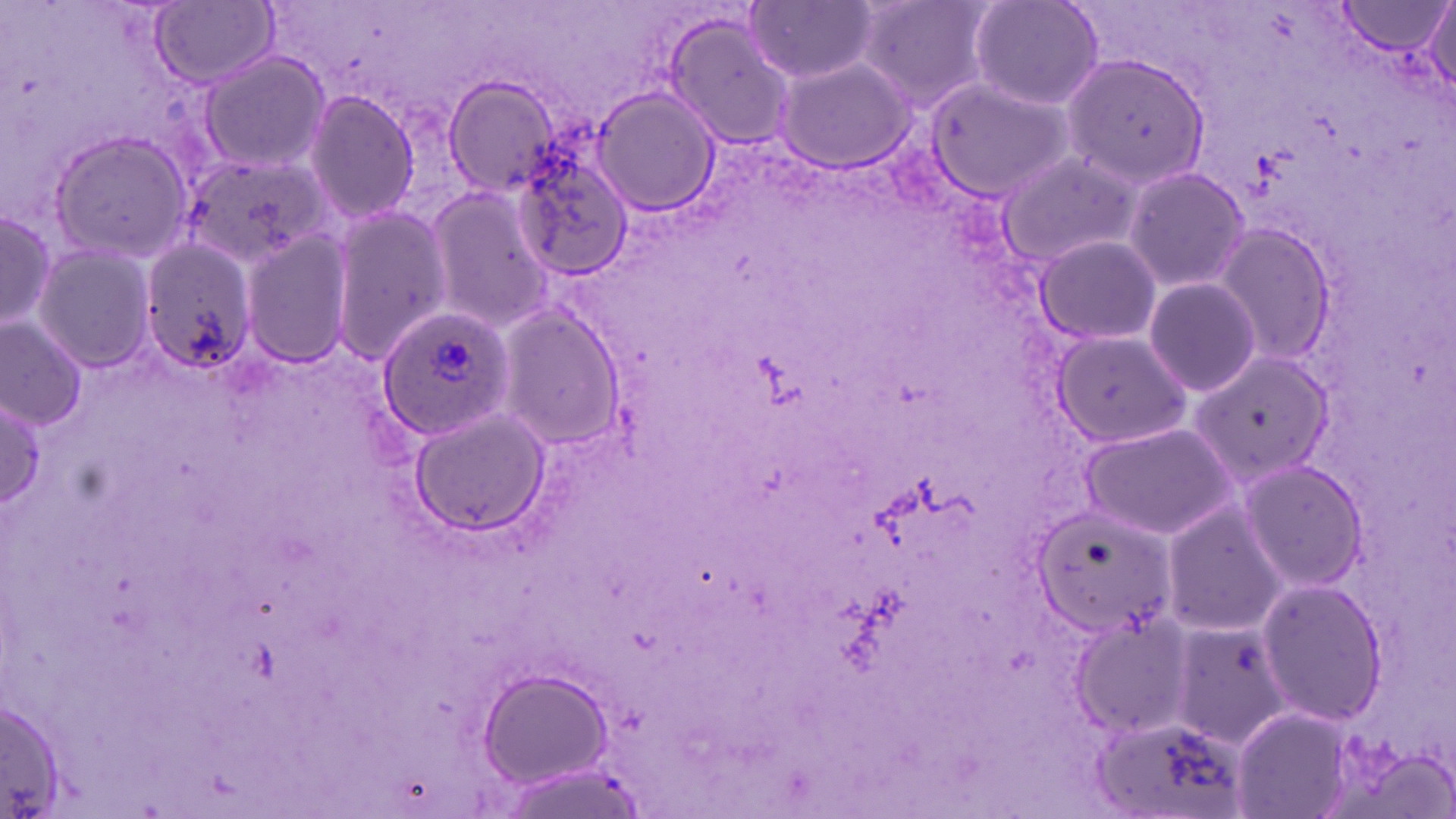

Approximate bounding boxes as (x1,y1)-(x2,y2) corner pairs in pixels. Uninfected red blood cell locations: (854,0)-(995,107), (966,0)-(1104,111), (149,1)-(279,88), (1338,1)-(1452,58), (747,2)-(879,83), (1422,3)-(1456,103), (662,13)-(798,151), (198,51)-(330,174), (1064,54)-(1208,189), (773,56)-(918,173), (924,71)-(1078,204), (444,75)-(565,198), (591,87)-(721,214), (301,91)-(421,224), (47,128)-(194,266), (998,149)-(1140,271), (180,154)-(333,268), (515,158)-(635,279), (1121,165)-(1249,293), (422,184)-(550,327), (0,203)-(56,340), (328,205)-(452,365), (1211,223)-(1339,365), (241,228)-(354,370), (1034,234)-(1161,346), (141,239)-(256,378), (29,245)-(159,374), (1143,276)-(1264,399), (494,304)-(626,454), (1,317)-(87,428), (1050,328)-(1192,448), (1189,351)-(1331,487), (1,397)-(48,508), (413,406)-(546,538), (1080,422)-(1234,536), (1235,459)-(1367,592), (1162,502)-(1284,634), (1032,506)-(1177,640), (1253,578)-(1388,726), (1071,614)-(1198,738), (1169,622)-(1290,747), (480,672)-(613,788), (0,700)-(65,812), (1093,710)-(1244,819). Plasmodium ovale-infected red blood cell locations: (377,302)-(516,437). Slide-level diagnosis: Plasmodium ovale. Optical microscopy. Single field of view. May-Grünwald-Giemsa-stained preparation. Thin blood film. Image is 1456×819 pixels. 1000x magnification.